Report the malaria status of this cell.
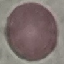
Uninfected.

Summary:
  - Image type: cell patch, automatically extracted from a larger field of view and resized to 64 × 64 pixels
  - Preparation: thin smear
  - Stain: Giemsa
  - Capture: smartphone through the microscope eyepiece